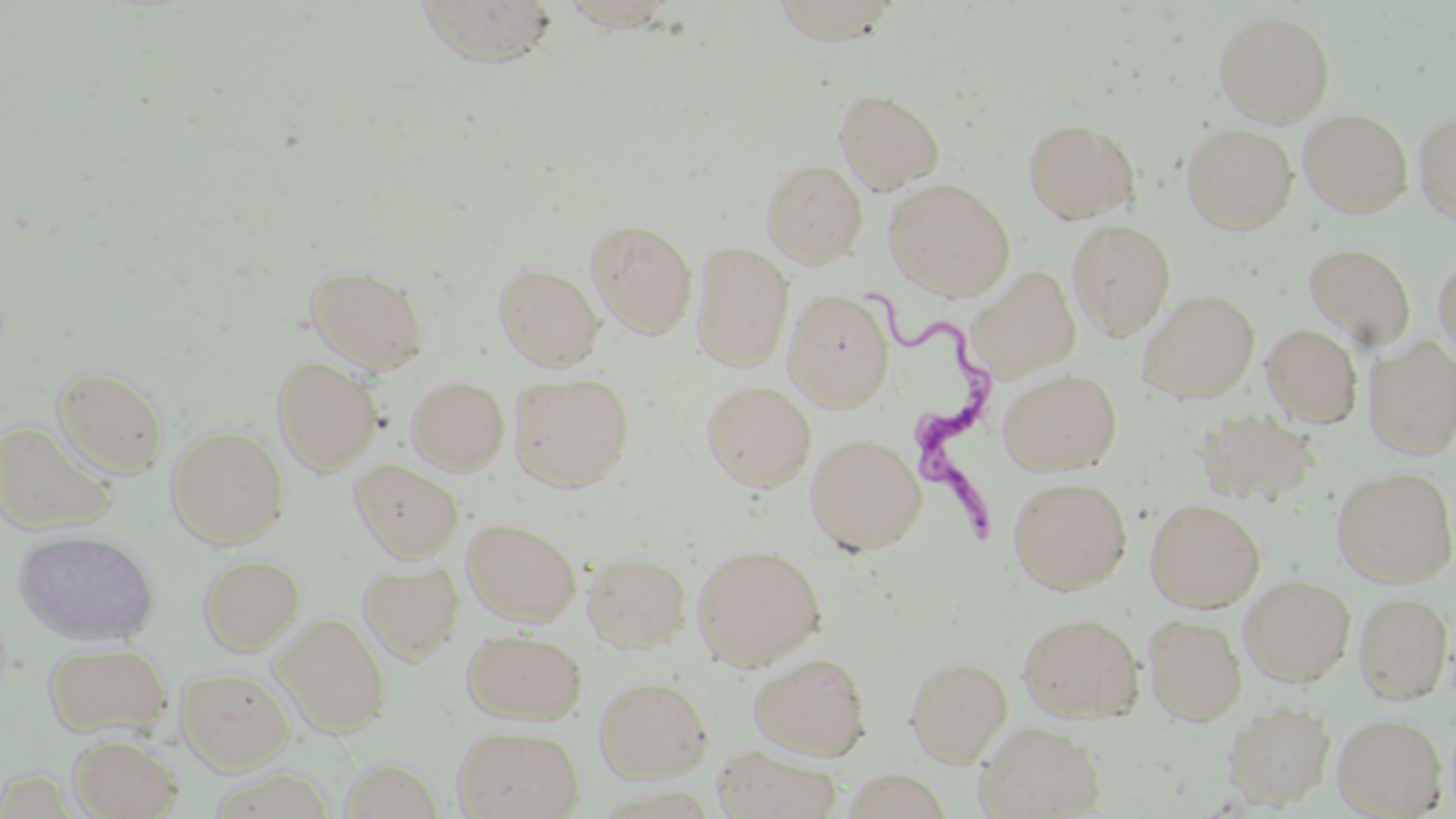

Summary:
  - Coordinate format: approximate bounding boxes as [x1, y1, x2, y2] in pixels
  - Uninfected red blood cell locations: [769, 0, 900, 44], [414, 1, 560, 68], [1212, 9, 1335, 125], [834, 87, 945, 193], [1298, 108, 1413, 217], [1414, 110, 1456, 223], [1022, 117, 1141, 223], [1181, 123, 1298, 234], [760, 158, 868, 268], [884, 178, 1015, 299], [586, 218, 698, 340], [1067, 219, 1176, 340], [691, 241, 794, 370], [1303, 242, 1416, 347], [1433, 254, 1456, 367], [493, 262, 604, 371], [306, 263, 430, 373], [971, 266, 1081, 379], [783, 289, 895, 409], [1137, 289, 1260, 402], [1261, 324, 1363, 427], [1363, 336, 1456, 458], [271, 355, 383, 474], [51, 365, 170, 478], [998, 368, 1122, 475], [509, 371, 635, 492], [406, 375, 510, 475], [701, 379, 816, 491], [1193, 407, 1320, 506], [0, 419, 117, 534], [166, 425, 289, 547], [805, 433, 927, 554], [350, 459, 464, 561], [1332, 466, 1456, 586], [1007, 475, 1132, 593], [1145, 497, 1266, 611], [462, 517, 580, 625], [13, 529, 160, 646], [692, 544, 826, 669], [582, 551, 691, 652], [198, 553, 305, 654], [358, 561, 464, 662], [1239, 574, 1356, 686], [1353, 591, 1454, 704], [1017, 610, 1145, 722], [274, 613, 390, 737], [1144, 613, 1247, 725], [462, 628, 587, 724], [43, 641, 172, 738], [748, 650, 872, 759], [905, 655, 1013, 765], [177, 667, 293, 774], [594, 674, 712, 781], [1222, 698, 1336, 808], [1333, 713, 1446, 817], [973, 720, 1106, 818], [452, 725, 584, 819], [68, 734, 182, 819], [714, 744, 842, 819], [842, 769, 951, 818]
  - Trypanosoma brucei locations: [859, 277, 1004, 564]
  - Slide-level diagnosis: Trypanosoma brucei
  - Magnification: 1000x
  - Preparation: thin blood film
  - Modality: light microscopy
  - Field of view: one of a larger specimen
  - Image size: 1456×819 pixels
  - Stain: May-Grünwald-Giemsa